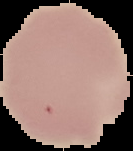
From a thin blood film. Cell region segmented out of the field of view; the surrounding area is masked to black. Malaria status: uninfected. Image is 133×151 pixels.